Assess the morphology of the erythrocytes.
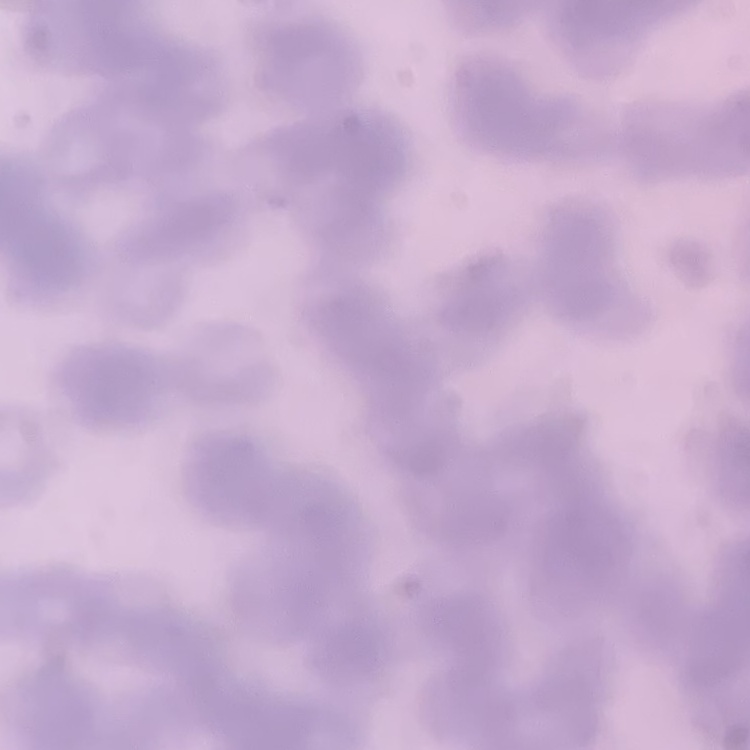

They show rouleaux formation.

Square crop of a larger photomicrograph. Stained with either Field's or Giemsa. Thin peripheral smear.